Identify the blood parasite species.
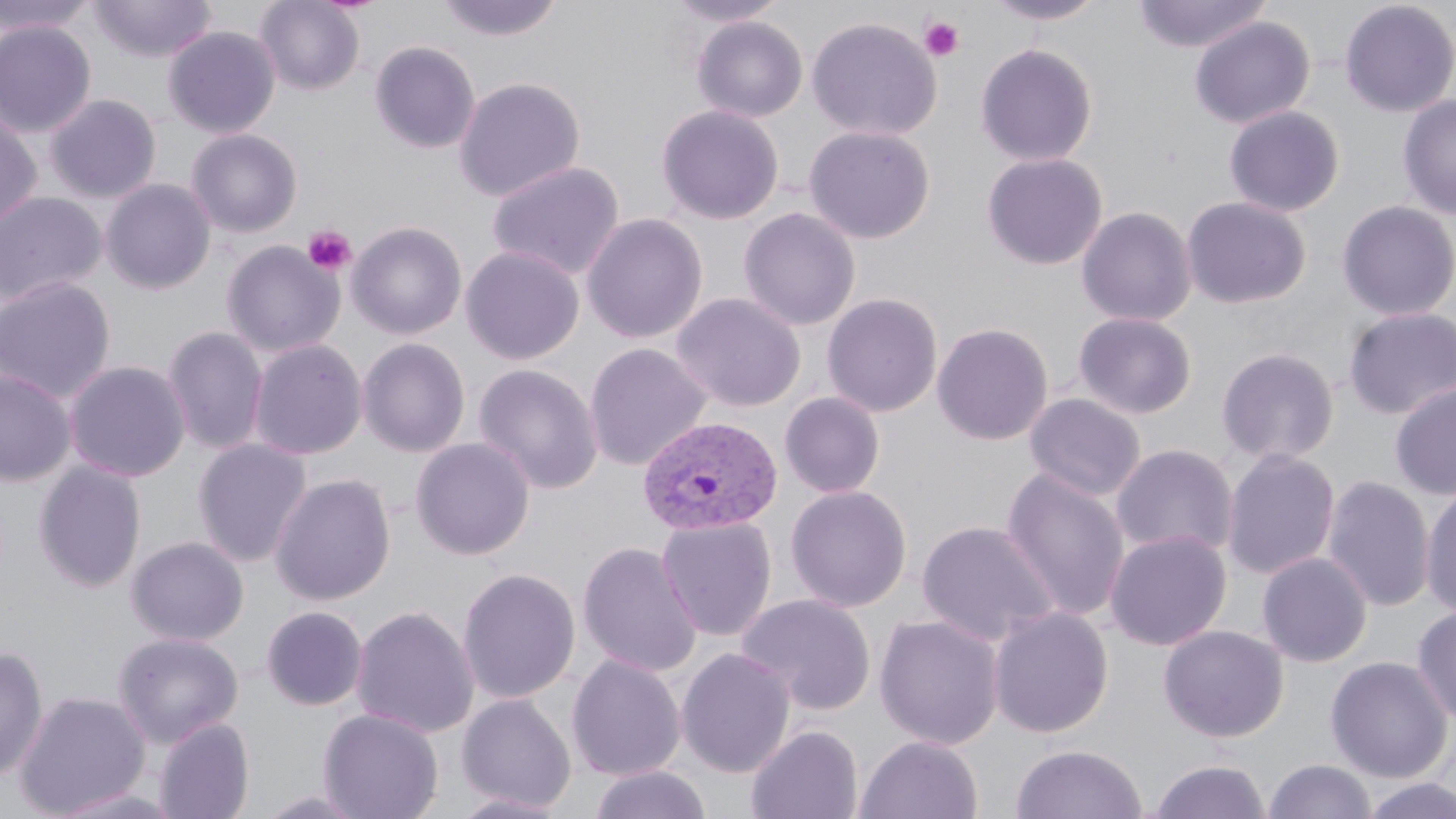

Plasmodium vivax.

Approximate bounding boxes as named x1/y1/x2/y2 corners in pixels. Uninfected red blood cell locations: (x1=0, y1=0, x2=97, y2=36), (x1=89, y1=0, x2=217, y2=62), (x1=254, y1=0, x2=366, y2=96), (x1=434, y1=0, x2=566, y2=42), (x1=663, y1=0, x2=789, y2=26), (x1=984, y1=0, x2=1107, y2=25), (x1=1132, y1=0, x2=1271, y2=53), (x1=1339, y1=1, x2=1456, y2=117), (x1=691, y1=16, x2=808, y2=122), (x1=1189, y1=16, x2=1315, y2=129), (x1=806, y1=17, x2=942, y2=141), (x1=0, y1=21, x2=97, y2=137), (x1=163, y1=26, x2=280, y2=138), (x1=369, y1=41, x2=480, y2=154), (x1=975, y1=43, x2=1098, y2=166), (x1=453, y1=77, x2=586, y2=202), (x1=45, y1=93, x2=162, y2=203), (x1=1398, y1=95, x2=1456, y2=220), (x1=656, y1=104, x2=784, y2=225), (x1=1223, y1=105, x2=1346, y2=217), (x1=0, y1=112, x2=43, y2=231), (x1=804, y1=125, x2=935, y2=244), (x1=185, y1=128, x2=303, y2=238), (x1=981, y1=152, x2=1108, y2=270), (x1=486, y1=161, x2=625, y2=281), (x1=100, y1=179, x2=216, y2=294), (x1=0, y1=191, x2=108, y2=308), (x1=1182, y1=196, x2=1311, y2=309), (x1=1336, y1=200, x2=1456, y2=321), (x1=1076, y1=206, x2=1197, y2=327), (x1=737, y1=207, x2=861, y2=331), (x1=582, y1=213, x2=708, y2=344), (x1=346, y1=221, x2=467, y2=340), (x1=221, y1=240, x2=344, y2=358), (x1=461, y1=245, x2=585, y2=365), (x1=0, y1=276, x2=116, y2=403), (x1=671, y1=292, x2=806, y2=412), (x1=822, y1=293, x2=943, y2=417), (x1=1342, y1=307, x2=1456, y2=420), (x1=1073, y1=312, x2=1198, y2=419), (x1=932, y1=322, x2=1053, y2=445), (x1=163, y1=326, x2=268, y2=455), (x1=357, y1=337, x2=470, y2=457), (x1=248, y1=338, x2=367, y2=460), (x1=584, y1=342, x2=711, y2=471), (x1=1216, y1=347, x2=1340, y2=465), (x1=64, y1=360, x2=190, y2=482), (x1=473, y1=363, x2=603, y2=494), (x1=0, y1=369, x2=76, y2=486), (x1=1389, y1=381, x2=1456, y2=501), (x1=779, y1=392, x2=885, y2=498), (x1=1024, y1=393, x2=1146, y2=502), (x1=410, y1=437, x2=535, y2=560), (x1=192, y1=438, x2=313, y2=567), (x1=1111, y1=443, x2=1238, y2=560), (x1=1222, y1=448, x2=1340, y2=580), (x1=33, y1=460, x2=147, y2=593), (x1=1001, y1=467, x2=1131, y2=623), (x1=270, y1=473, x2=396, y2=605), (x1=1322, y1=475, x2=1435, y2=612), (x1=1421, y1=483, x2=1456, y2=620), (x1=785, y1=485, x2=912, y2=612), (x1=656, y1=516, x2=777, y2=641), (x1=917, y1=520, x2=1061, y2=647), (x1=1105, y1=529, x2=1231, y2=651), (x1=126, y1=536, x2=249, y2=646), (x1=577, y1=541, x2=702, y2=677), (x1=1257, y1=552, x2=1372, y2=667), (x1=457, y1=567, x2=581, y2=703), (x1=735, y1=593, x2=877, y2=716), (x1=351, y1=605, x2=479, y2=738), (x1=1411, y1=605, x2=1456, y2=726), (x1=261, y1=606, x2=368, y2=711), (x1=988, y1=606, x2=1113, y2=738), (x1=874, y1=614, x2=1004, y2=750), (x1=1158, y1=624, x2=1288, y2=743), (x1=112, y1=630, x2=244, y2=747), (x1=0, y1=646, x2=49, y2=783), (x1=676, y1=647, x2=796, y2=778), (x1=567, y1=654, x2=686, y2=781), (x1=1325, y1=656, x2=1453, y2=783), (x1=14, y1=690, x2=151, y2=817), (x1=455, y1=693, x2=577, y2=813), (x1=318, y1=708, x2=444, y2=819), (x1=153, y1=717, x2=255, y2=819), (x1=746, y1=724, x2=863, y2=819), (x1=854, y1=734, x2=984, y2=819), (x1=1010, y1=744, x2=1147, y2=819), (x1=1147, y1=759, x2=1272, y2=819), (x1=1262, y1=759, x2=1377, y2=818), (x1=587, y1=765, x2=713, y2=819), (x1=1358, y1=776, x2=1456, y2=819), (x1=47, y1=785, x2=184, y2=819), (x1=252, y1=789, x2=373, y2=819), (x1=445, y1=793, x2=571, y2=819). Platelet locations: (x1=919, y1=16, x2=964, y2=61), (x1=302, y1=225, x2=356, y2=275). Plasmodium vivax-infected red blood cell locations: (x1=638, y1=416, x2=783, y2=536). 1000x magnification. One field of a larger specimen. Thin blood smear. May-Grünwald-Giemsa-stained preparation. Optical microscopy. Image is 1456×819 pixels.